Assess this cell for malaria.
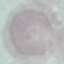

It is uninfected.

Summary:
  - Preparation: thin blood film
  - Image type: cell patch, automatically extracted from a larger field of view and resized to 64 × 64 pixels
  - Stain: Giemsa
  - Capture: smartphone through the microscope eyepiece